Comment on the morphology of the erythrocytes.
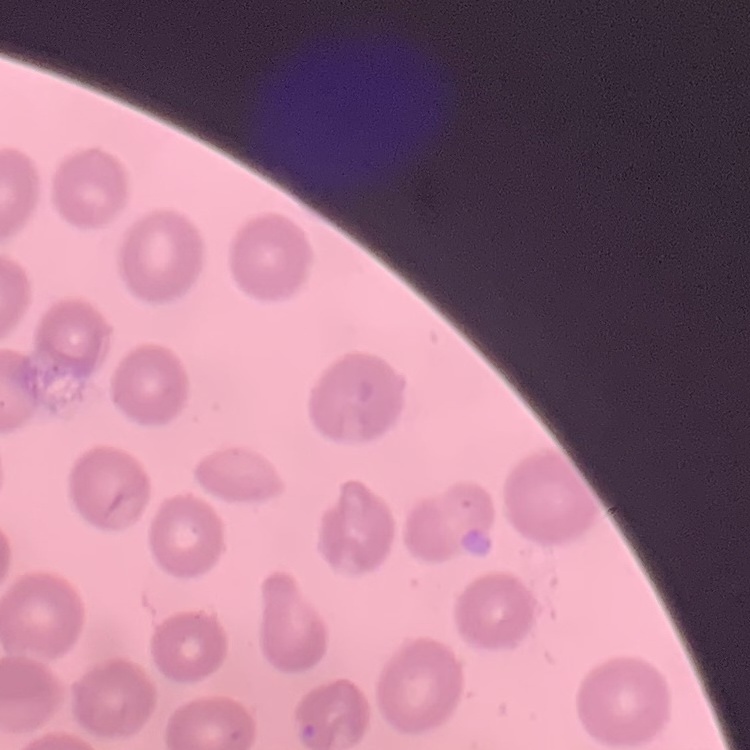

No rouleaux formation.

Square crop of a larger photomicrograph. Stained with either Field's or Giemsa. Thin peripheral smear.